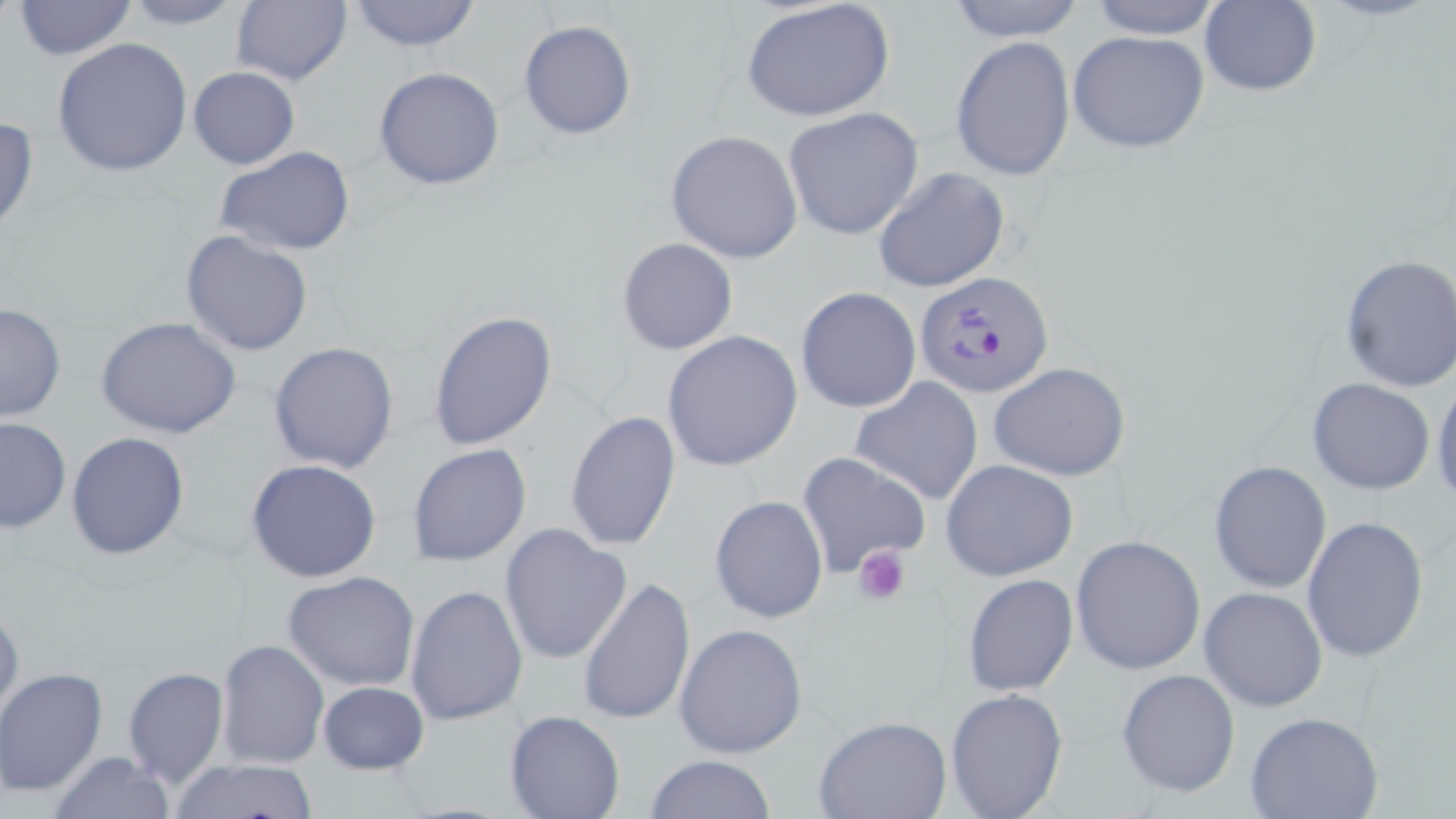

{
  "slide_level_diagnosis": "Plasmodium falciparum",
  "preparation": "thin blood smear",
  "modality": "optical microscopy",
  "stain": "May-Grünwald-Giemsa",
  "magnification": "1000x",
  "platelet_locations": "approximate bounding boxes as named x1/y1/x2/y2 corners in pixels: (x1=852, y1=544, x2=911, y2=605)",
  "field_of_view": "single",
  "uninfected_red_blood_cell_locations": "approximate bounding boxes as named x1/y1/x2/y2 corners in pixels: (x1=119, y1=0, x2=250, y2=29), (x1=230, y1=0, x2=352, y2=87), (x1=344, y1=0, x2=483, y2=52), (x1=740, y1=0, x2=896, y2=123), (x1=942, y1=0, x2=1088, y2=42), (x1=1083, y1=0, x2=1227, y2=40), (x1=13, y1=1, x2=138, y2=59), (x1=1199, y1=2, x2=1321, y2=97), (x1=519, y1=20, x2=636, y2=139), (x1=1067, y1=30, x2=1211, y2=154), (x1=951, y1=35, x2=1076, y2=182), (x1=52, y1=37, x2=192, y2=178), (x1=374, y1=66, x2=507, y2=190), (x1=188, y1=67, x2=299, y2=169), (x1=782, y1=107, x2=924, y2=240), (x1=0, y1=113, x2=39, y2=238), (x1=666, y1=130, x2=803, y2=265), (x1=215, y1=145, x2=356, y2=257), (x1=872, y1=168, x2=1010, y2=294), (x1=181, y1=231, x2=313, y2=356), (x1=616, y1=236, x2=738, y2=355), (x1=1337, y1=252, x2=1456, y2=397), (x1=795, y1=286, x2=921, y2=414), (x1=0, y1=302, x2=64, y2=423), (x1=429, y1=309, x2=559, y2=453), (x1=97, y1=316, x2=242, y2=441), (x1=660, y1=329, x2=804, y2=471), (x1=268, y1=341, x2=400, y2=473), (x1=988, y1=361, x2=1133, y2=482), (x1=1431, y1=370, x2=1456, y2=513), (x1=850, y1=376, x2=985, y2=505), (x1=1306, y1=377, x2=1436, y2=495), (x1=564, y1=410, x2=680, y2=552), (x1=0, y1=417, x2=70, y2=532), (x1=66, y1=431, x2=192, y2=560), (x1=407, y1=444, x2=532, y2=567), (x1=797, y1=450, x2=932, y2=577), (x1=246, y1=458, x2=382, y2=583), (x1=941, y1=458, x2=1079, y2=581), (x1=1208, y1=460, x2=1332, y2=595), (x1=709, y1=494, x2=829, y2=624), (x1=1301, y1=516, x2=1429, y2=663), (x1=499, y1=523, x2=632, y2=666), (x1=1070, y1=534, x2=1206, y2=675), (x1=282, y1=570, x2=422, y2=692), (x1=962, y1=574, x2=1078, y2=697), (x1=578, y1=577, x2=695, y2=728), (x1=405, y1=583, x2=528, y2=726), (x1=1199, y1=587, x2=1328, y2=712), (x1=0, y1=601, x2=23, y2=729), (x1=673, y1=622, x2=807, y2=759), (x1=217, y1=639, x2=329, y2=768), (x1=122, y1=666, x2=229, y2=790), (x1=1116, y1=668, x2=1240, y2=798), (x1=1, y1=669, x2=108, y2=797), (x1=316, y1=680, x2=430, y2=775), (x1=945, y1=686, x2=1069, y2=818), (x1=505, y1=711, x2=625, y2=819), (x1=1246, y1=712, x2=1385, y2=819), (x1=814, y1=714, x2=951, y2=818), (x1=47, y1=752, x2=178, y2=819), (x1=646, y1=754, x2=777, y2=819), (x1=168, y1=758, x2=322, y2=818)",
  "image_size": "1456×819 pixels",
  "plasmodium_falciparum_infected_red_blood_cell_locations": "approximate bounding boxes as named x1/y1/x2/y2 corners in pixels: (x1=914, y1=268, x2=1055, y2=398)"
}